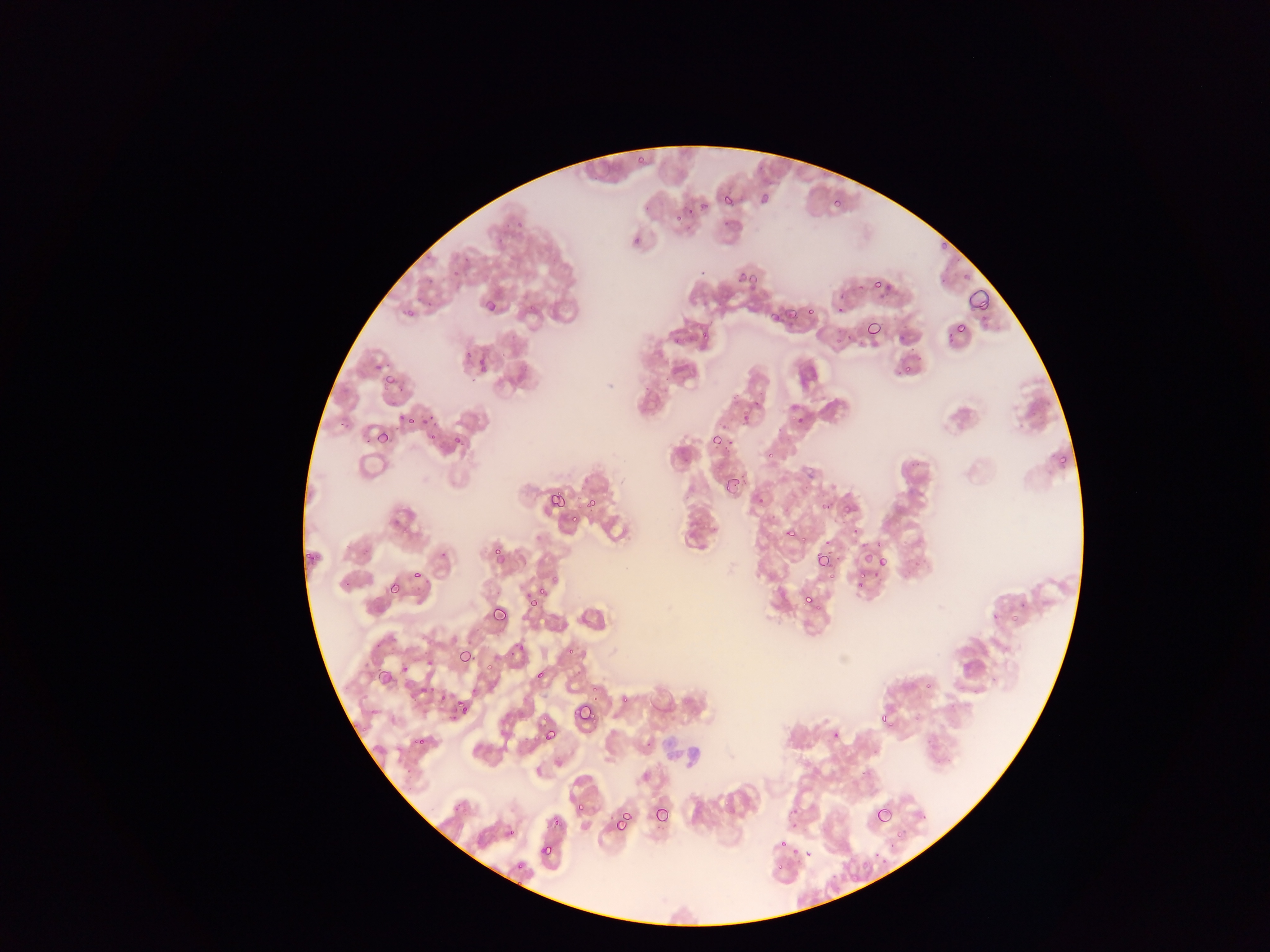
country = Ghana
field of view = single
preparation = thin blood smear
malaria parasite locations = approximate bounding boxes as {left, top, right, bottom} in pixels: {634, 154, 648, 169}, {760, 192, 770, 203}, {721, 193, 735, 206}, {831, 194, 844, 210}, {698, 200, 709, 212}, {680, 202, 697, 218}, {675, 205, 692, 222}, {938, 240, 951, 252}, {736, 271, 751, 285}, {871, 277, 887, 292}, {968, 289, 988, 311}, {483, 299, 500, 313}, {807, 303, 820, 314}, {805, 306, 815, 316}, {402, 307, 416, 320}, {771, 307, 791, 326}, {865, 319, 882, 335}, {954, 321, 967, 334}, {699, 328, 711, 341}, {475, 356, 491, 374}, {900, 364, 912, 375}, {387, 374, 404, 393}, {397, 411, 414, 428}, {421, 411, 436, 427}, {376, 428, 392, 442}, {450, 432, 464, 447}, {710, 434, 724, 448}, {766, 447, 778, 459}, {1054, 453, 1068, 467}, {723, 473, 744, 492}, {547, 487, 568, 511}, {753, 492, 766, 507}, {585, 496, 599, 509}, {820, 499, 835, 512}, {839, 500, 855, 516}, {568, 514, 578, 524}, {783, 526, 799, 541}, {824, 538, 838, 549}, {491, 543, 508, 562}, {814, 549, 832, 568}, {305, 551, 318, 564}, {876, 555, 891, 567}, {853, 561, 871, 582}, {411, 569, 423, 581}, {855, 570, 868, 585}, {384, 578, 401, 597}, {527, 580, 551, 601}, {524, 591, 540, 606}, {802, 593, 817, 608}, {489, 606, 508, 624}, {564, 644, 574, 655}, {457, 649, 473, 665}, {424, 658, 435, 669}, {483, 660, 491, 674}, {374, 666, 396, 687}, {534, 667, 547, 681}, {922, 680, 935, 691}, {591, 683, 606, 698}, {437, 689, 449, 701}, {617, 693, 629, 705}, {457, 703, 468, 714}, {574, 703, 592, 721}, {879, 713, 892, 726}, {541, 729, 555, 742}, {829, 730, 840, 740}, {417, 735, 428, 747}, {872, 801, 891, 820}, {573, 802, 586, 816}, {653, 803, 672, 824}, {613, 812, 632, 833}, {548, 814, 563, 831}, {505, 827, 514, 838}, {893, 831, 906, 840}, {777, 840, 787, 849}, {540, 844, 552, 857}, {514, 863, 523, 872}
capture = mobile-phone photograph through a microscope
image size = 1270×952 pixels